State the preparation type.
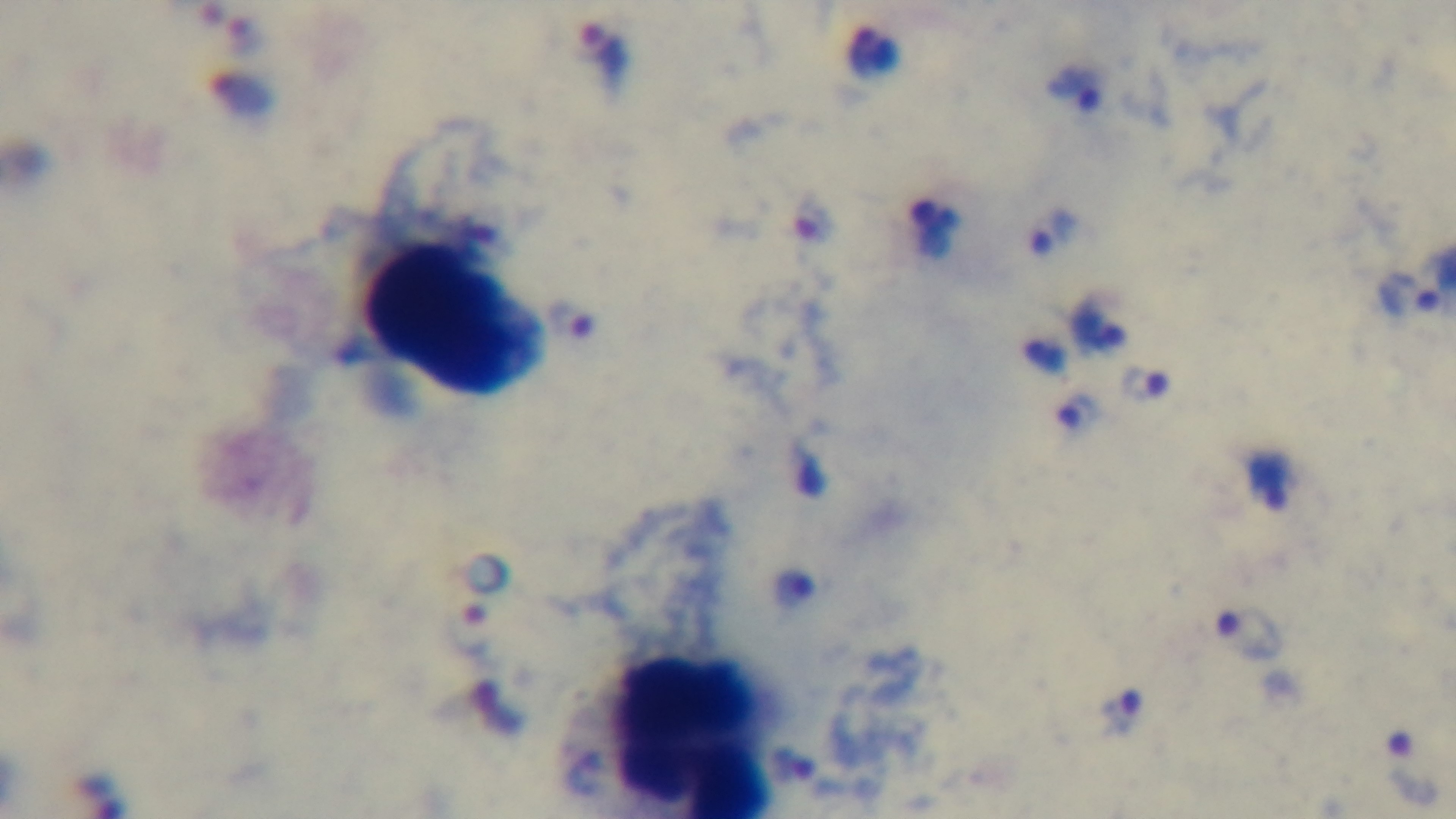

Thick.

Giemsa-stained. Oil-immersion objective, 100x. Photomicrograph. Malaria status: infected. Captured with a mounted 4K digital camera. One field from the slide.